Report the malaria status.
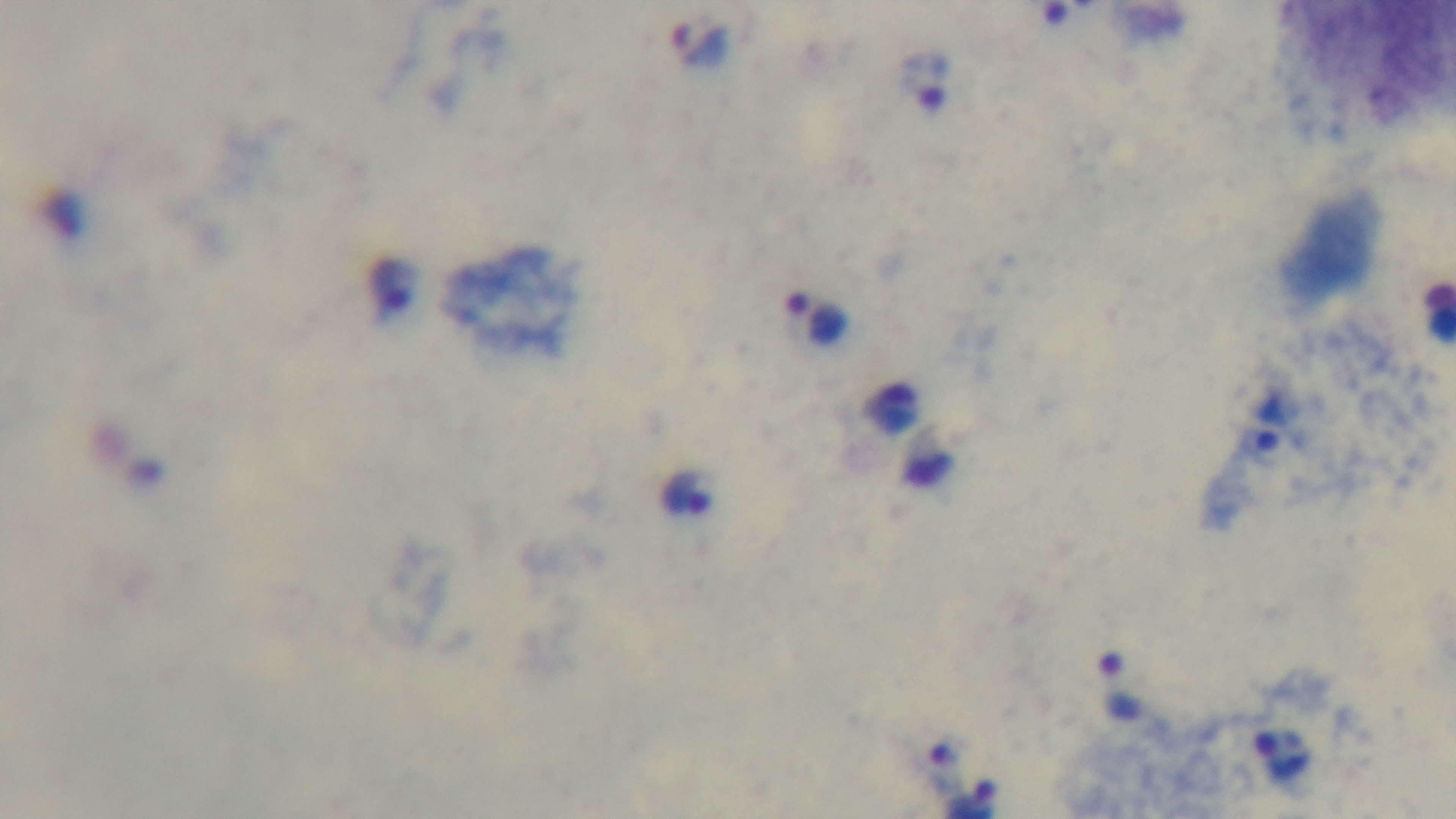

Positive.

Summary:
  - Objective: 100x oil immersion
  - Field of view: single
  - Stain: Giemsa
  - Capture: mounted 4K digital camera
  - Preparation: thick blood film
  - Modality: light microscopy